Assess this cell for malaria.
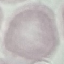

Uninfected.

Cell patch, automatically extracted from a larger field of view and resized to 64 × 64 pixels. Acquired by smartphone through the microscope eyepiece. Thin blood film. Giemsa-stained preparation.